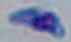
{
  "identification": "Toxoplasma gondii",
  "modality": "micrograph",
  "magnification": "1000x"
}